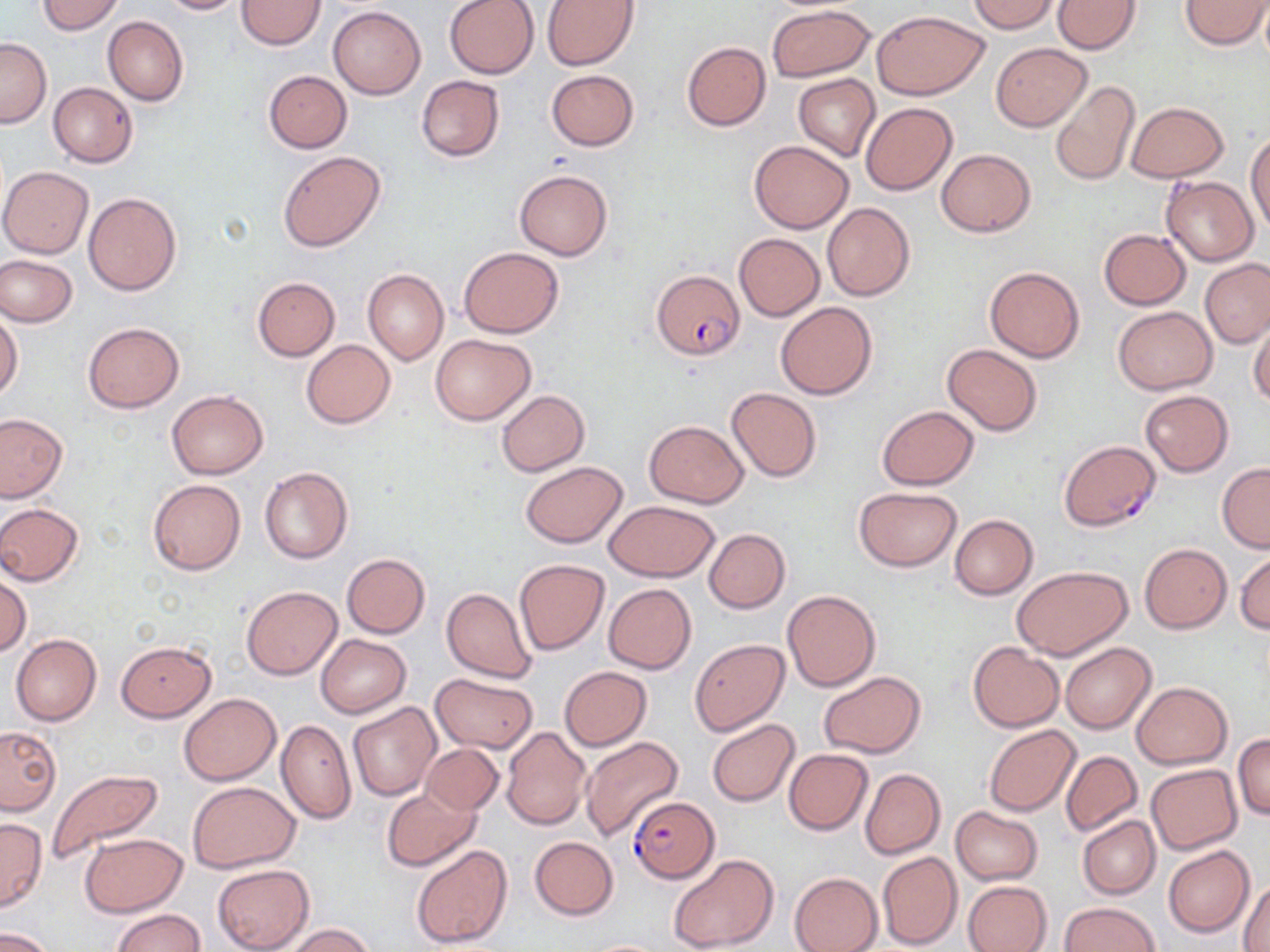
Summary:
  - Coordinate format: approximate bounding boxes as (x1,y1)-(x2,y2) corner pairs in pixels
  - Plasmodium falciparum-infected red blood cell locations: (651,269)-(745,360), (1059,439)-(1162,531), (627,795)-(718,882)
  - Uninfected red blood cell locations: (37,0)-(124,34), (155,0)-(244,14), (443,0)-(539,79), (542,0)-(639,69), (971,0)-(1059,34), (1053,0)-(1141,54), (1179,0)-(1269,50), (237,1)-(325,50), (1258,3)-(1270,64), (766,4)-(875,83), (328,5)-(426,99), (872,10)-(988,100), (103,16)-(188,105), (0,38)-(51,128), (682,41)-(771,131), (991,43)-(1090,131), (546,69)-(638,151), (264,70)-(351,152), (793,74)-(880,162), (415,75)-(506,162), (1050,80)-(1141,186), (48,82)-(138,167), (1127,100)-(1228,182), (860,102)-(958,195), (1247,130)-(1270,234), (749,140)-(854,233), (936,148)-(1035,237), (278,149)-(385,252), (0,165)-(94,258), (514,169)-(613,261), (1161,177)-(1257,265), (83,192)-(181,296), (821,202)-(915,301), (1100,228)-(1190,310), (734,233)-(825,321), (459,246)-(564,338), (0,254)-(78,327), (1201,258)-(1270,348), (984,266)-(1085,363), (363,269)-(449,366), (252,277)-(340,360), (775,301)-(877,398), (1113,307)-(1217,394), (0,311)-(23,402), (1248,313)-(1270,407), (83,322)-(184,413), (430,334)-(536,424), (301,340)-(396,429), (941,342)-(1043,436), (726,387)-(823,481), (166,390)-(269,479), (495,390)-(589,476), (1141,390)-(1234,476), (876,405)-(979,490), (0,413)-(67,502), (643,420)-(750,507), (520,462)-(627,548), (1217,463)-(1270,552), (259,467)-(353,564), (148,480)-(245,575), (854,486)-(964,572), (603,501)-(720,581), (0,503)-(84,585), (949,514)-(1038,599), (704,528)-(790,613), (1139,543)-(1231,632), (1235,551)-(1270,634), (341,553)-(430,638), (513,559)-(609,655), (1011,565)-(1132,660), (0,573)-(31,656), (603,583)-(697,674), (242,586)-(342,679), (441,587)-(536,682), (782,589)-(881,691), (10,634)-(102,726), (314,634)-(411,718), (689,639)-(789,735), (115,640)-(216,722), (967,642)-(1064,732), (1059,643)-(1156,733), (560,667)-(651,750), (821,671)-(926,758), (430,672)-(539,752), (1132,682)-(1232,769), (179,692)-(280,786), (348,702)-(439,800), (276,720)-(357,824), (707,720)-(801,806), (984,725)-(1081,816), (0,726)-(62,815), (501,726)-(590,831), (1233,733)-(1270,820), (579,736)-(683,842), (421,743)-(503,816), (783,749)-(873,834), (1060,751)-(1142,836), (1147,764)-(1241,854), (47,767)-(163,862), (860,768)-(944,858), (188,782)-(300,872), (381,788)-(481,871), (950,807)-(1042,884), (1078,815)-(1160,899), (0,818)-(46,911), (79,834)-(188,917), (529,836)-(618,920), (410,843)-(514,950), (1164,845)-(1254,938), (877,852)-(962,949), (668,853)-(780,950), (212,864)-(314,952), (789,872)-(882,952), (1238,878)-(1270,952), (963,880)-(1052,952), (1058,902)-(1159,952), (112,908)-(204,952), (284,923)-(375,952), (2,927)-(58,951)
  - Slide-level diagnosis: Plasmodium falciparum
  - Image size: 1270×952 pixels
  - Preparation: thin blood film
  - Field of view: one of a larger specimen
  - Stain: May-Grünwald-Giemsa
  - Magnification: 1000x
  - Modality: light microscopy